Classify this cell by malaria status.
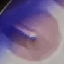

Uninfected.

capture = smartphone camera at the microscope eyepiece
stain = Giemsa
image type = cell patch, automatically extracted from a larger field of view and resized to 64 × 64 pixels
preparation = thin blood film